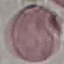 Result: negative for malaria parasites. Photographed with a smartphone camera at the microscope eyepiece. Thin blood film. Giemsa stain. Cell patch, automatically extracted from a larger field of view and resized to 64 × 64 pixels.